State which parasite is depicted.
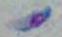

This is Toxoplasma gondii.

Summary:
  - Modality: photomicrograph
  - Magnification: 1000x